Classify this cell by malaria status.
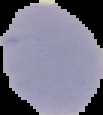
It is uninfected.

Image is 103×115 pixels. From a thin blood smear. Cell region segmented out of the field of view; the surrounding area is masked to black.